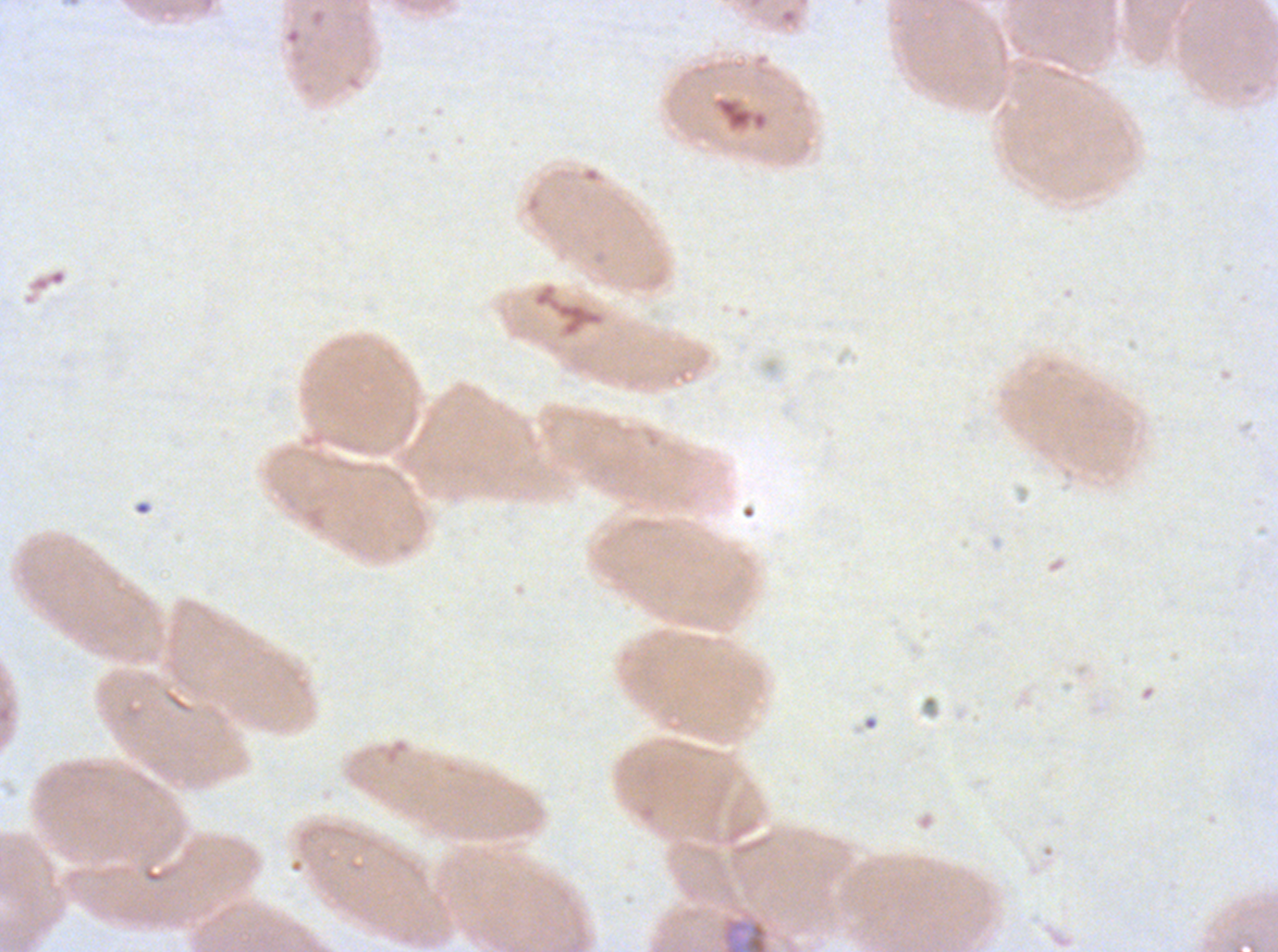
Approximate bounding boxes as [x1, y1, x2, y2] in pixels. Mid trophozoite locations: [722, 918, 769, 951]. Ex-vivo Plasmodium falciparum culture from a patient in The Gambia, grown for 24 to 48 hours. Thin blood smear. A sub-image separated from a larger composite. Image is 1278×952 pixels. Giemsa stain.